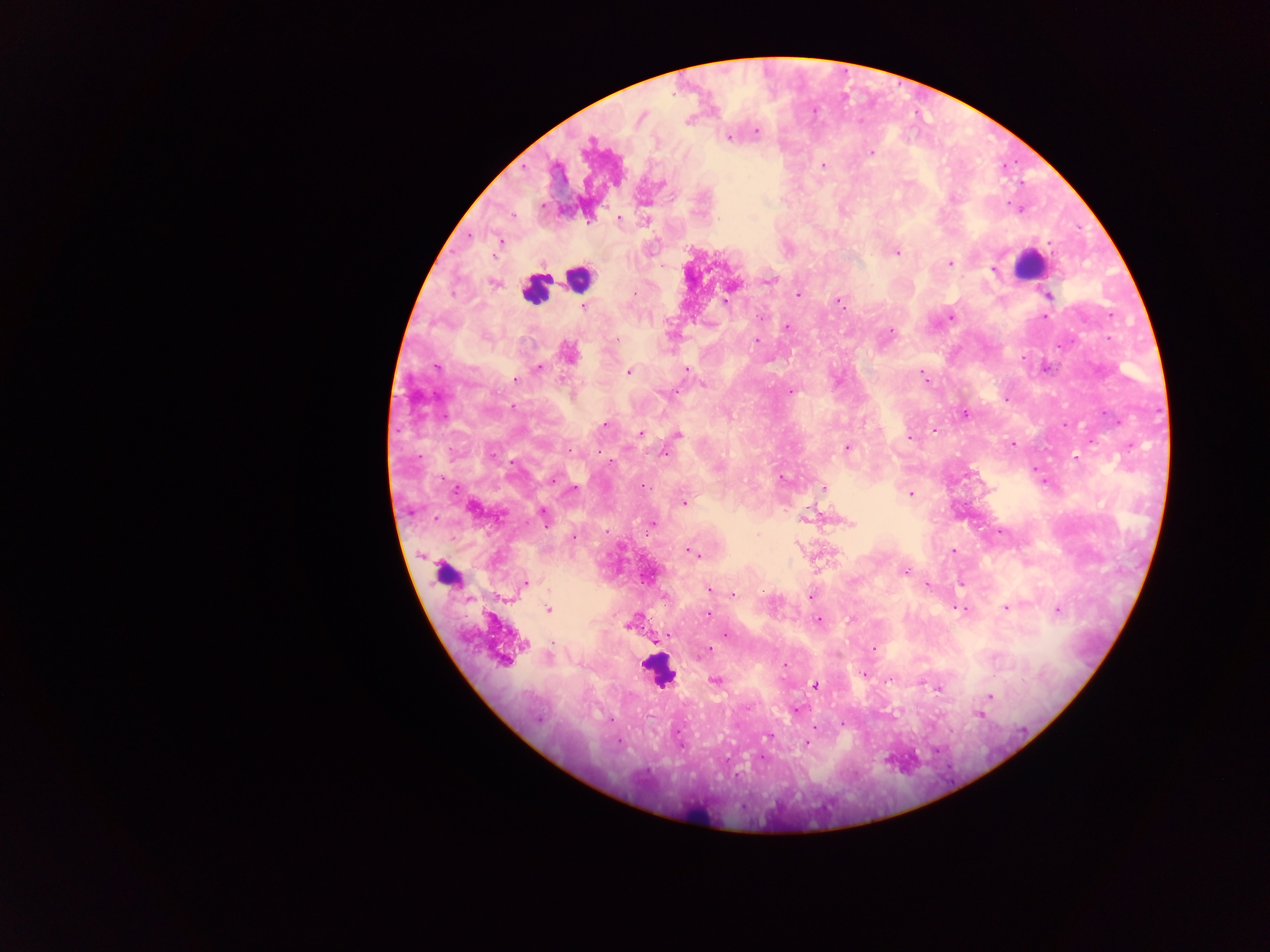
Approximate centers as (x, y) in pixels. Malaria parasite locations: (641, 117), (688, 121), (756, 131), (729, 137), (870, 152), (823, 165), (661, 184), (618, 217), (499, 240), (896, 252), (949, 264), (994, 269), (769, 280), (493, 282), (730, 287), (797, 295), (1048, 295), (838, 300), (583, 306), (950, 317), (1044, 317), (786, 328), (890, 331), (757, 341), (567, 352), (538, 368), (685, 369), (630, 371), (923, 378), (515, 379), (703, 384), (790, 391), (1006, 398), (964, 414), (1065, 423), (605, 424), (933, 431), (640, 433), (677, 434), (909, 439), (1091, 439), (1011, 444), (1129, 445), (846, 447), (664, 452), (1076, 457), (553, 478), (782, 478), (823, 488), (572, 490), (910, 493), (683, 502), (472, 507), (543, 514), (804, 519), (849, 523), (651, 524), (572, 536), (953, 550), (691, 552), (904, 572), (525, 583), (926, 584), (710, 589), (715, 591), (731, 594), (811, 596), (1006, 607), (961, 609), (1057, 609), (548, 610), (709, 614), (819, 620), (631, 622), (669, 635), (727, 635), (873, 648), (708, 649), (504, 659), (785, 665), (864, 674), (890, 678), (715, 679), (814, 685), (938, 688), (990, 695), (795, 708), (980, 714), (842, 724), (767, 735), (807, 742). Object labeled both malaria parasite and leukocyte by the source: (446, 575). Leukocyte locations: (1030, 264), (578, 277), (534, 289), (658, 670), (698, 815). Sample from Ghana. Single field of view. Thick blood film. Image is 1270×952 pixels. Photographed through a microscope with a mobile-phone camera.